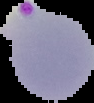

Summary:
  - Image type: cell region segmented out of the field of view; surrounding area masked to black
  - Preparation: thin blood smear
  - Image size: 94×103 pixels
  - Result: malaria parasites identified